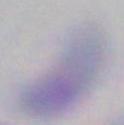
Summary:
  - Modality: photomicrograph
  - Magnification: 1000x
  - Identification: Toxoplasma gondii